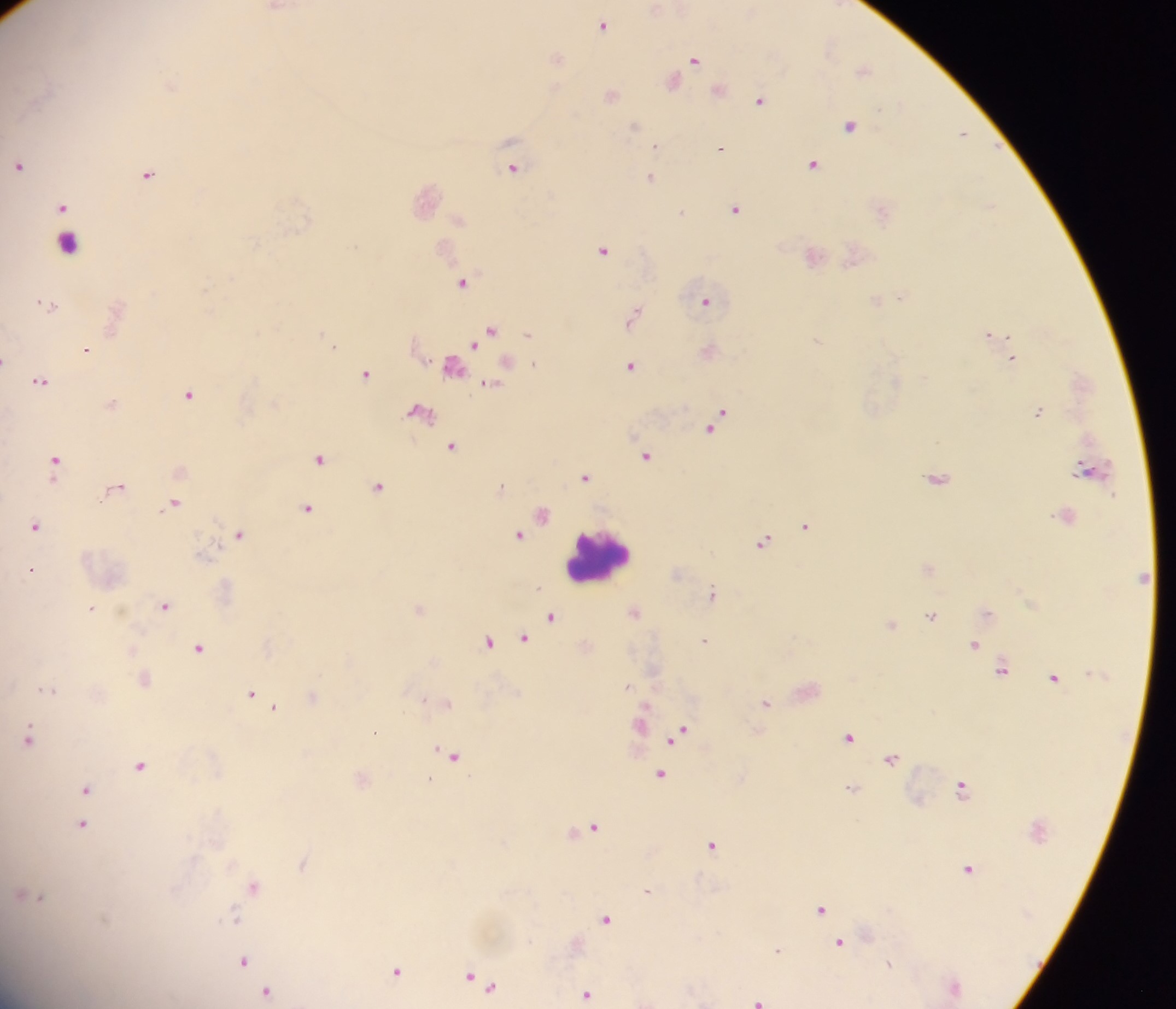 Approximate centers as x y in pixels. Leukocyte locations: 69 242; 599 556. Plasmodium parasite locations: 603 24; 557 57; 695 58; 863 69; 673 81; 760 99; 850 125; 962 132; 656 144; 720 147; 813 162; 19 164; 512 168; 149 174; 651 177; 991 205; 62 207; 736 208; 683 211; 603 249; 463 281; 900 295; 705 300; 49 304; 634 313; 490 331; 992 333; 334 344; 87 349; 1013 358; 4 359; 631 365; 366 373; 40 380; 490 384; 189 393; 1039 412; 718 420; 452 445; 646 455; 320 457; 56 461; 585 476; 938 477; 118 485; 379 485; 175 503; 307 506; 542 514; 36 524; 805 525; 239 533; 518 534; 763 541; 32 569; 712 592; 165 604; 91 607; 419 608; 635 611; 932 615; 552 616; 892 624; 525 637; 705 639; 488 641; 975 643; 200 648; 1002 667; 1054 677; 627 685; 49 689; 252 694; 313 696; 422 699; 447 701; 766 702; 274 706; 643 714; 375 731; 679 733; 30 736; 850 736; 452 755; 891 758; 141 764; 660 773; 429 779; 962 786; 851 787; 86 788; 83 824; 593 825; 712 844; 303 861; 969 868; 255 885; 648 889; 31 894; 821 908; 233 916; 606 918; 840 942; 778 949; 244 960; 889 963; 396 970; 470 976; 482 981; 953 986; 266 990; 587 993; 758 1000. Sample from Ghana. Single field of view. Mobile-phone photograph taken through the microscope. Thick blood film. Image is 1176×1009 pixels.